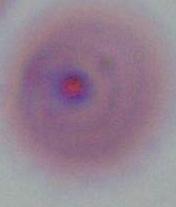
Summary:
  - Magnification: 400x or 1000x
  - Modality: photomicrograph
  - Identification: Plasmodium